Identify the cell.
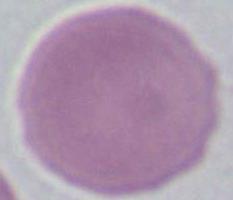

This is an erythrocyte.

Summary:
  - Magnification: 1000x
  - Modality: micrograph